Identify the parasite.
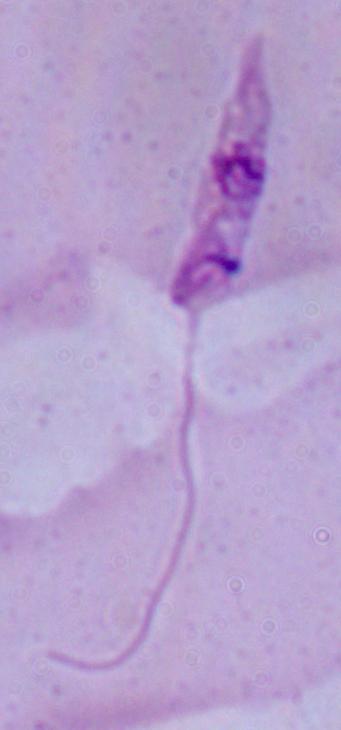
This is Leishmania.

Micrograph. 1000x magnification.